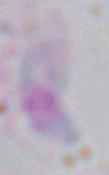 Micrograph. Toxoplasma gondii is shown. 1000x magnification.